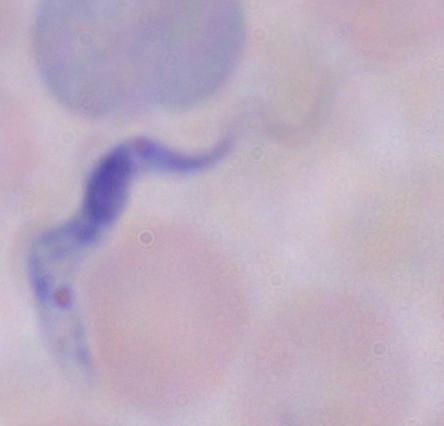
magnification = 1000x
modality = micrograph
identification = trypanosome